Classify this cell by malaria status.
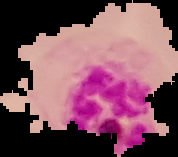

It is parasitized.

Summary:
  - Preparation: thin blood smear
  - Image size: 178×157 pixels
  - Image type: segmented cell region with the area outside set to black